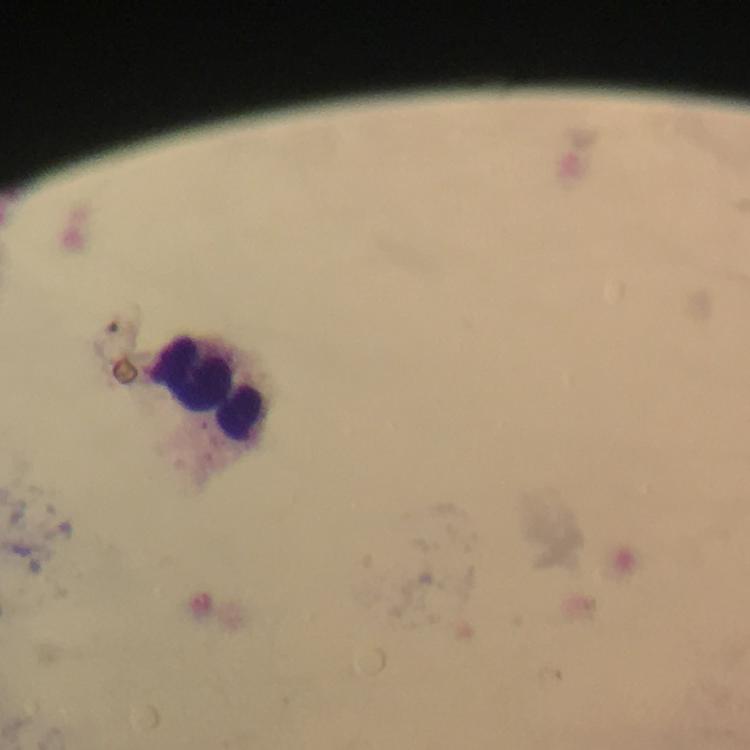
Approximate centers as [x, y] in pixels.
Summary:
  - Leukocyte locations: [205, 390]
  - Context: from a malaria diagnostic workup
  - Malaria parasites: none detected
  - Preparation: thick smear
  - Magnification: 100x
  - Stain: Giemsa
  - Image size: 750×750 pixels
  - Capture: smartphone photograph through a microscope
  - Cropped from: one field of view
  - Immersion oil: applied